Assess this cell for malaria.
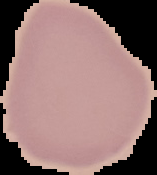
Uninfected.

From a thin blood film. Image is 157×175 pixels. The area outside the segmented cell region is set to black.